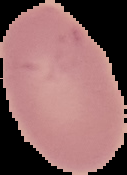

image type = segmented cell region on a black background
image size = 127×175 pixels
preparation = thin blood film
result = no Plasmodium parasites seen